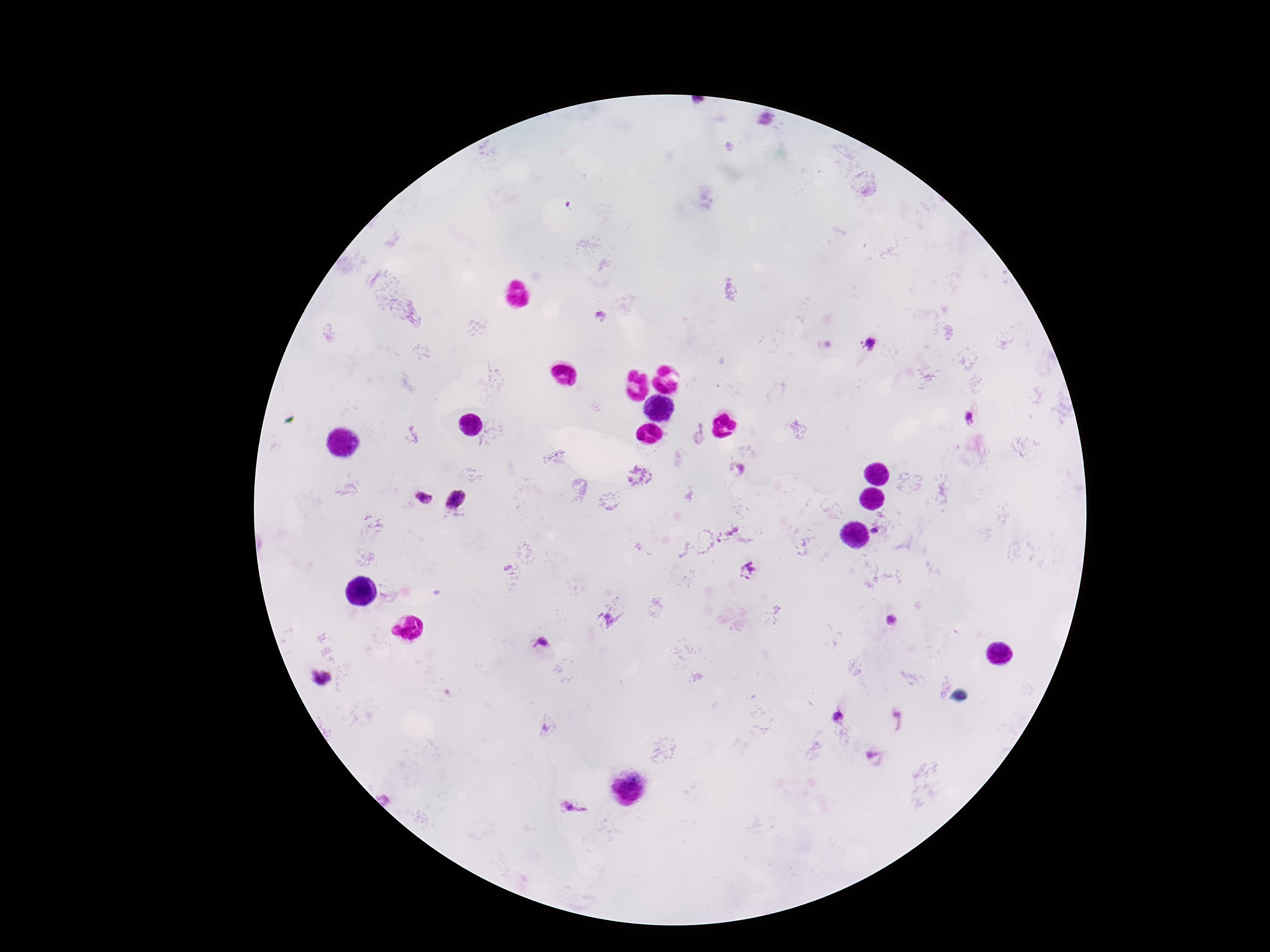 Approximate centers as [x, y] in pixels. Plasmodium parasite locations: [767, 123], [601, 318], [868, 345], [972, 420], [737, 470], [639, 477], [424, 496], [456, 500], [875, 531], [726, 534], [747, 571], [892, 621], [540, 643], [321, 678], [838, 717], [574, 809]. Thick blood film. Single field of view. Patient malaria status: positive. Photographed through the microscope eyepiece with a smartphone camera. Image is 1270×952 pixels. Giemsa-stained preparation. 100x magnification.